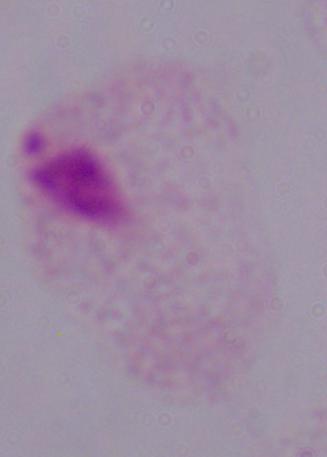
magnification = 1000x
identification = trichomonad
modality = micrograph